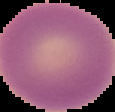
Summary:
  - Preparation: thin blood smear
  - Result: no malaria parasites detected
  - Image size: 115×112 pixels
  - Image type: cell region segmented out of the field of view; surrounding area masked to black